Report the malaria status of this cell.
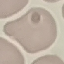
Uninfected.

stain = Giemsa
capture = smartphone through the microscope eyepiece
image type = cell patch, automatically extracted from a larger field of view and resized to 64 × 64 pixels
preparation = thin blood film